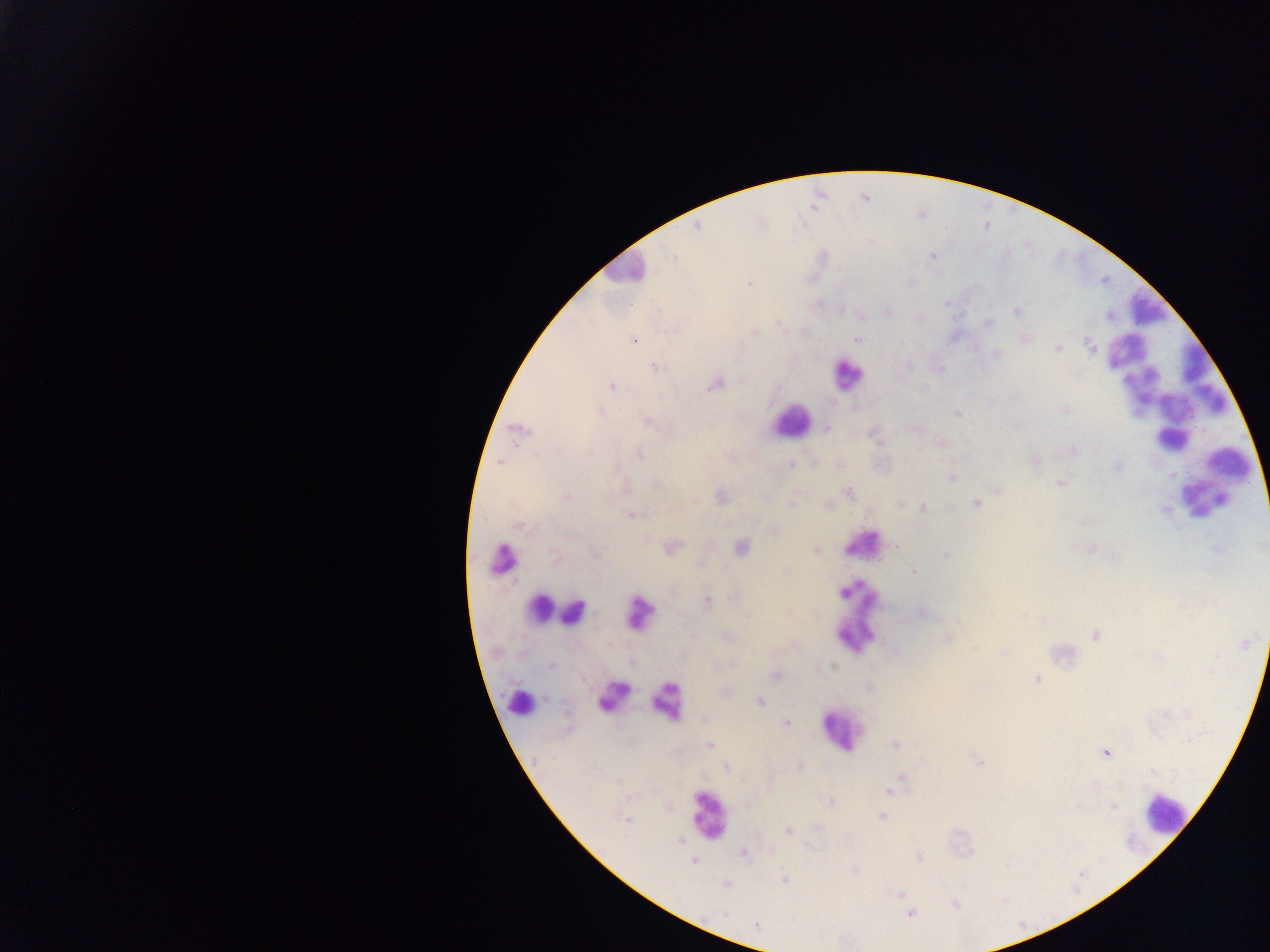
Approximate centers as (x, y) in pixels.
Summary:
  - Malaria parasite locations: (697, 227), (673, 255), (933, 256), (748, 283), (1017, 311), (989, 322), (857, 339), (633, 340), (1090, 345), (1057, 349), (998, 354), (655, 367), (715, 385), (612, 386), (1065, 410), (601, 411), (957, 414), (648, 421), (826, 429), (520, 431), (875, 435), (1073, 451), (590, 452), (639, 454), (1035, 461), (499, 462), (791, 465), (1116, 466), (952, 477), (657, 484), (1060, 484), (997, 491), (849, 493), (721, 497), (566, 498), (694, 500), (791, 503), (976, 503), (900, 504), (922, 508), (1164, 509), (633, 515), (518, 524), (774, 531), (896, 546), (673, 547), (740, 547), (1091, 549), (816, 550), (598, 555), (946, 555), (914, 571), (707, 602), (926, 613), (747, 616), (1096, 636), (949, 638), (1245, 643), (733, 663), (550, 666), (776, 674), (1037, 678), (869, 687), (759, 701), (703, 719), (787, 723), (895, 744), (710, 745), (1106, 753), (980, 762), (800, 766), (727, 769), (901, 776), (897, 782), (889, 791), (830, 802), (1114, 806), (882, 816), (627, 820), (789, 830), (680, 840), (743, 853), (919, 857), (693, 861), (855, 870), (784, 879), (726, 885), (900, 894), (956, 905), (724, 913), (910, 913), (757, 925)
  - Leukocyte locations (subset; some below the resolvable size): (623, 269), (1146, 307), (1125, 350), (847, 376), (1199, 378), (1140, 388), (791, 420), (1178, 424), (1232, 466), (1204, 497), (865, 542), (502, 558), (540, 607), (573, 612), (859, 612), (638, 613), (615, 692), (667, 700), (522, 701), (839, 730), (1164, 813), (708, 814)
  - Preparation: thick blood film
  - Image size: 1270×952 pixels
  - Capture: mobile-phone photograph through a microscope
  - Field of view: single
  - Country: Ghana